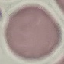

Summary:
  - Result: no malaria parasites detected
  - Preparation: thin smear
  - Capture: smartphone camera at the microscope eyepiece
  - Image type: cell patch, automatically extracted from a larger field of view and resized to 64 × 64 pixels
  - Stain: Giemsa